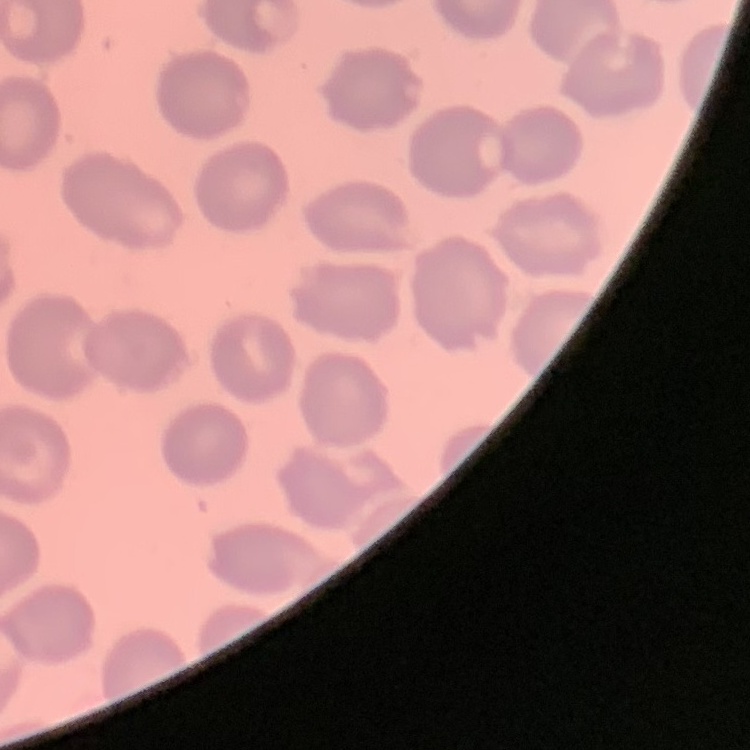
erythrocyte morphology = no rouleaux formation
stain = Field's or Giemsa
image type = square crop of a larger photomicrograph
preparation = thin blood smear